Report the malaria status of this cell.
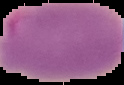

It is parasitized.

Segmented cell region on a black background. From a thin blood film. Image is 124×85 pixels.